Point out each malaria parasite.
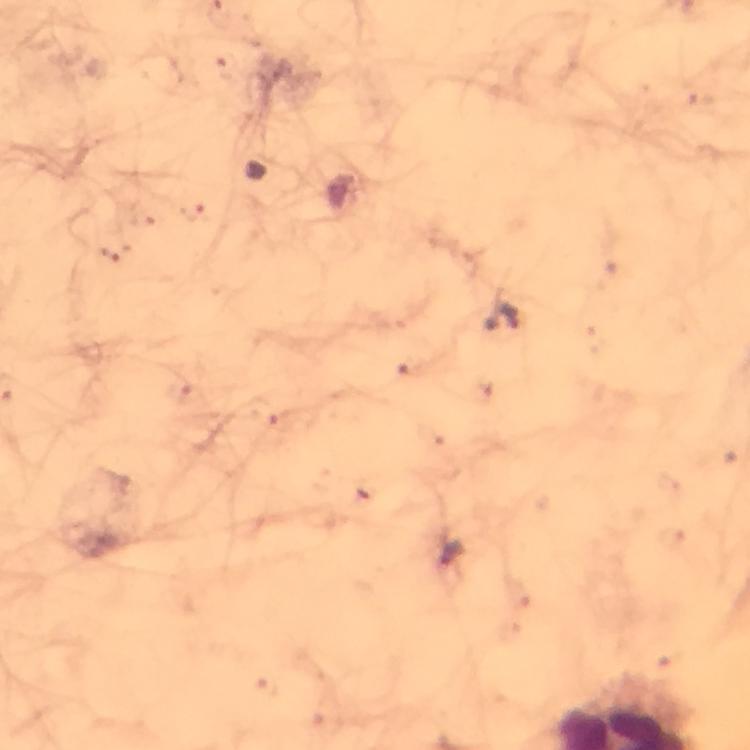

Approximate object centers, in pixels from the top-left corner.
Malaria parasites: (x=503, y=320), (x=450, y=556).

Summary:
  - Preparation: thick smear
  - Capture: smartphone camera through the microscope
  - Magnification: 100x
  - Context: from a diagnostic examination for malaria
  - Image size: 750×750 pixels
  - Cropped from: a single field of view
  - Immersion oil: used
  - Stain: Giemsa